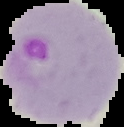
Result: Plasmodium parasites identified. Image is 124×127 pixels. From a thin blood film. The area outside the segmented cell region is set to black.